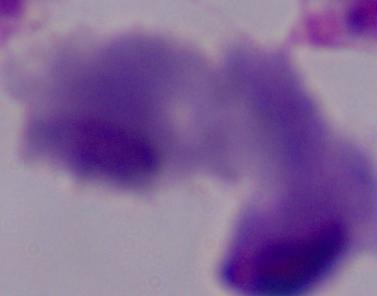

modality = photomicrograph
identification = trichomonad
magnification = 1000x